Classify this cell by malaria status.
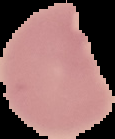

Uninfected.

From a thin blood film. Image is 115×139 pixels. Segmented cell region on a black background.